Comment on the morphology of the erythrocytes.
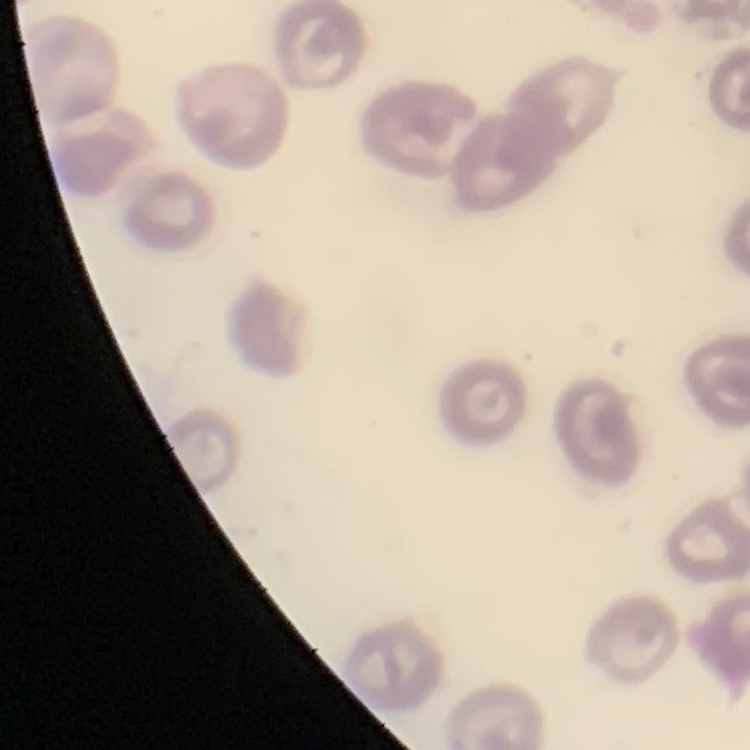
No rouleaux formation.

Summary:
  - Stain: Field's or Giemsa
  - Image type: square crop of a larger photomicrograph
  - Preparation: thin peripheral smear